Assess this cell for malaria.
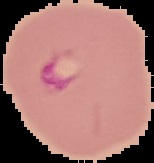
Parasitized.

Summary:
  - Preparation: thin blood smear
  - Image size: 154×163 pixels
  - Image type: segmented cell region on a black background